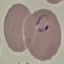

Summary:
  - Result: malaria parasites detected
  - Image type: automatically extracted cell patch, resized to 64 × 64 pixels
  - Stain: Giemsa
  - Capture: smartphone camera at the microscope eyepiece
  - Preparation: thin smear